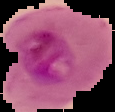
Summary:
  - Image type: segmented cell region on a black background
  - Image size: 115×112 pixels
  - Preparation: thin blood film
  - Malaria status: parasitized